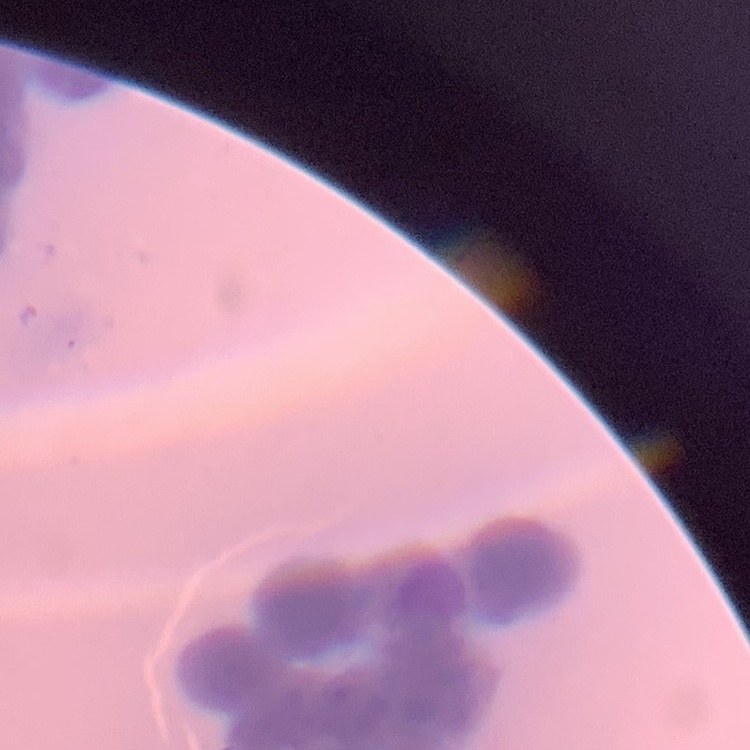

Summary:
  - Erythrocyte morphology: rouleaux formation
  - Image type: square crop of a larger photomicrograph
  - Stain: Field's or Giemsa
  - Preparation: thin blood smear